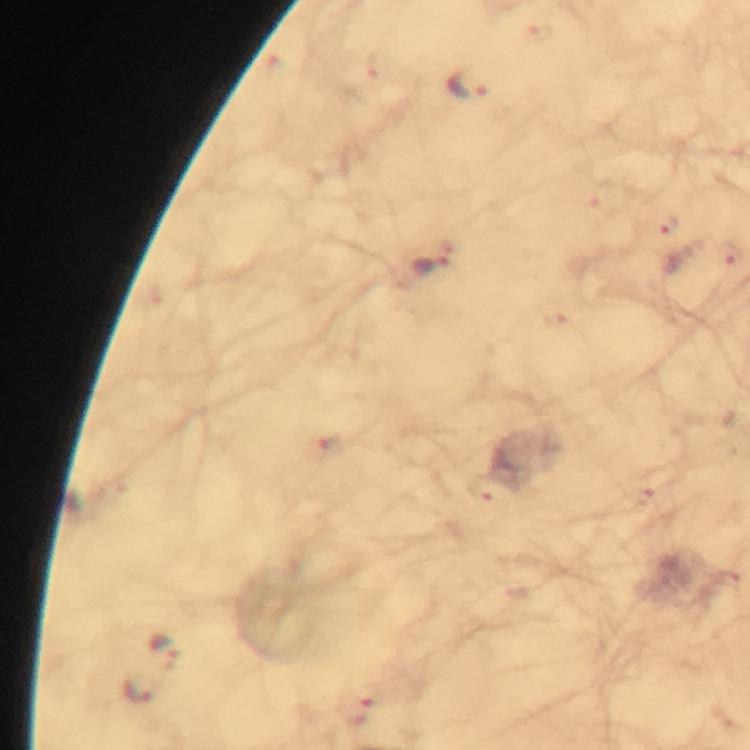
Approximate centers as [x, y] in pixels.
Summary:
  - Malaria parasite locations: [468, 87], [666, 227], [729, 254], [430, 265], [327, 447], [486, 492], [644, 497], [166, 650], [364, 692], [141, 693]
  - Capture: smartphone camera through the microscope
  - Image size: 750×750 pixels
  - Magnification: 100x
  - Context: from a malaria diagnostic workup
  - Cropped from: one field of view
  - Stain: Giemsa
  - Preparation: thick smear
  - Immersion oil: used